Assess this cell for malaria.
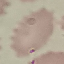

Uninfected.

Summary:
  - Stain: Giemsa
  - Preparation: thin smear
  - Capture: smartphone through the microscope eyepiece
  - Image type: cell patch, automatically extracted from a larger field of view and resized to 64 × 64 pixels